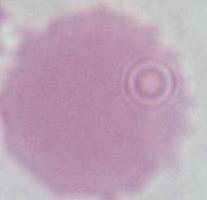 Photomicrograph. A red blood cell is seen. Captured at 1000x magnification.